Identify the blood parasite species.
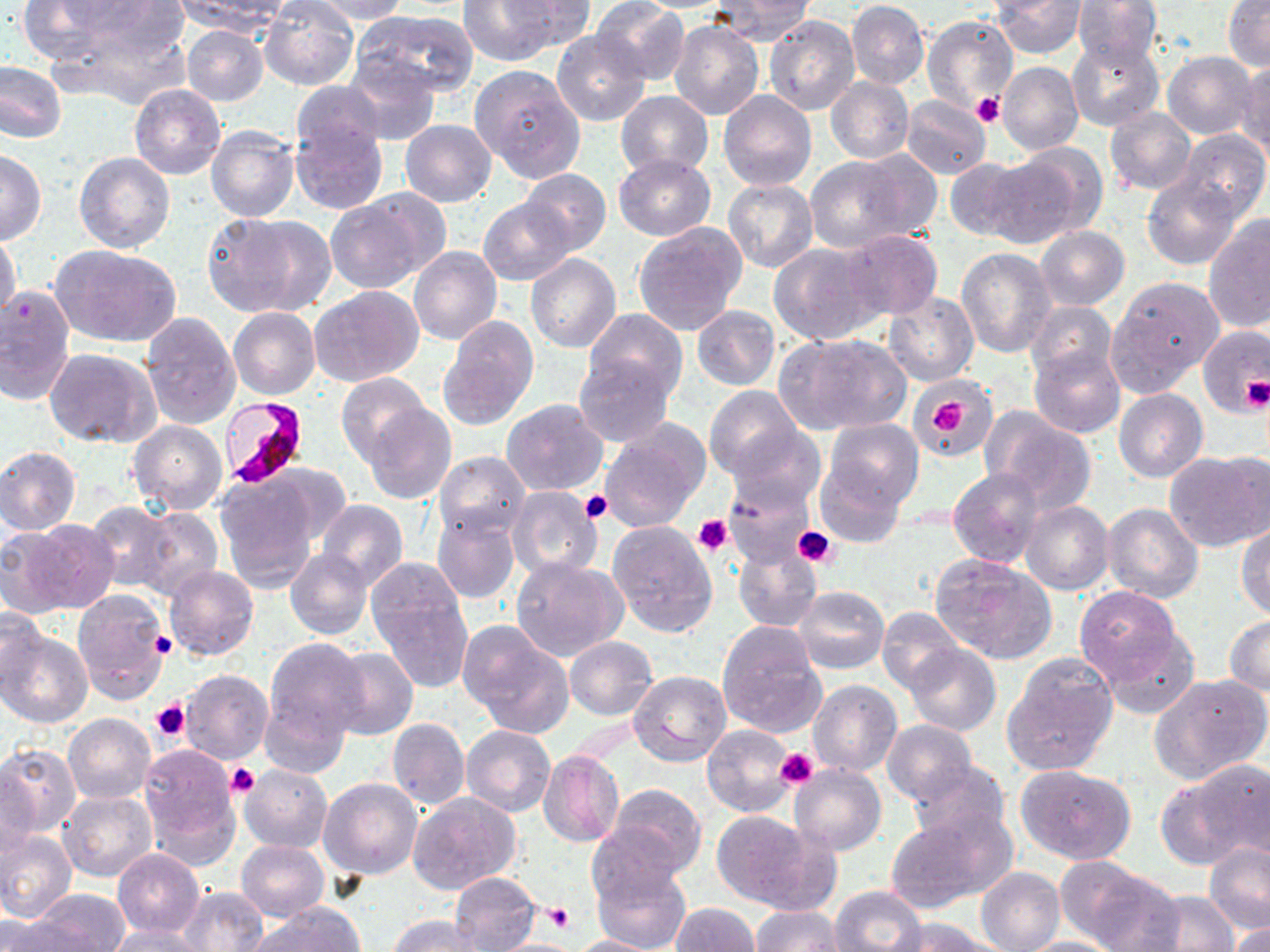
Plasmodium falciparum.

Summary:
  - Coordinate format: approximate bounding boxes as named x1/y1/x2/y2 corners in pixels
  - Uninfected red blood cell locations: (x1=16, y1=0, x2=116, y2=64), (x1=58, y1=0, x2=180, y2=53), (x1=259, y1=0, x2=359, y2=91), (x1=308, y1=0, x2=412, y2=23), (x1=456, y1=0, x2=562, y2=67), (x1=709, y1=0, x2=815, y2=45), (x1=992, y1=0, x2=1086, y2=58), (x1=1072, y1=0, x2=1162, y2=70), (x1=1223, y1=0, x2=1270, y2=70), (x1=175, y1=1, x2=292, y2=36), (x1=502, y1=1, x2=594, y2=49), (x1=592, y1=1, x2=690, y2=85), (x1=847, y1=1, x2=928, y2=89), (x1=352, y1=10, x2=478, y2=98), (x1=765, y1=15, x2=860, y2=115), (x1=922, y1=15, x2=1017, y2=113), (x1=668, y1=20, x2=765, y2=120), (x1=181, y1=25, x2=267, y2=107), (x1=551, y1=30, x2=651, y2=126), (x1=1066, y1=34, x2=1164, y2=131), (x1=1162, y1=50, x2=1259, y2=139), (x1=342, y1=56, x2=440, y2=146), (x1=0, y1=60, x2=66, y2=143), (x1=998, y1=60, x2=1084, y2=155), (x1=1236, y1=60, x2=1270, y2=154), (x1=471, y1=65, x2=585, y2=184), (x1=824, y1=77, x2=913, y2=164), (x1=289, y1=81, x2=385, y2=160), (x1=130, y1=83, x2=226, y2=179), (x1=719, y1=89, x2=816, y2=190), (x1=615, y1=91, x2=713, y2=178), (x1=902, y1=96, x2=990, y2=178), (x1=1104, y1=109, x2=1198, y2=195), (x1=400, y1=119, x2=496, y2=207), (x1=291, y1=122, x2=387, y2=215), (x1=206, y1=125, x2=299, y2=223), (x1=1178, y1=129, x2=1269, y2=220), (x1=985, y1=148, x2=1097, y2=248), (x1=0, y1=151, x2=45, y2=244), (x1=73, y1=152, x2=174, y2=254), (x1=612, y1=152, x2=716, y2=240), (x1=804, y1=156, x2=921, y2=253), (x1=944, y1=158, x2=1031, y2=242), (x1=519, y1=169, x2=610, y2=255), (x1=1142, y1=173, x2=1242, y2=269), (x1=723, y1=180, x2=819, y2=272), (x1=328, y1=192, x2=438, y2=292), (x1=478, y1=197, x2=576, y2=284), (x1=201, y1=211, x2=334, y2=319), (x1=1203, y1=218, x2=1270, y2=333), (x1=634, y1=222, x2=748, y2=335), (x1=1036, y1=225, x2=1129, y2=309), (x1=839, y1=229, x2=942, y2=321), (x1=0, y1=231, x2=20, y2=321), (x1=770, y1=241, x2=883, y2=344), (x1=52, y1=245, x2=181, y2=348), (x1=409, y1=245, x2=502, y2=344), (x1=956, y1=248, x2=1058, y2=358), (x1=525, y1=253, x2=621, y2=352), (x1=416, y1=260, x2=513, y2=410), (x1=1109, y1=277, x2=1221, y2=387), (x1=0, y1=284, x2=75, y2=405), (x1=309, y1=285, x2=423, y2=386), (x1=884, y1=291, x2=978, y2=387), (x1=1025, y1=300, x2=1118, y2=386), (x1=692, y1=306, x2=781, y2=390), (x1=228, y1=307, x2=319, y2=401), (x1=583, y1=307, x2=687, y2=402), (x1=139, y1=310, x2=241, y2=430), (x1=435, y1=315, x2=537, y2=432), (x1=1198, y1=324, x2=1270, y2=417), (x1=776, y1=333, x2=911, y2=436), (x1=1028, y1=346, x2=1124, y2=438), (x1=45, y1=348, x2=161, y2=449), (x1=572, y1=353, x2=673, y2=446), (x1=337, y1=373, x2=434, y2=468), (x1=913, y1=380, x2=999, y2=458), (x1=706, y1=386, x2=802, y2=481), (x1=1114, y1=388, x2=1208, y2=482), (x1=502, y1=398, x2=608, y2=495), (x1=361, y1=403, x2=456, y2=504), (x1=983, y1=409, x2=1096, y2=511), (x1=127, y1=419, x2=228, y2=515), (x1=822, y1=419, x2=922, y2=514), (x1=598, y1=420, x2=709, y2=531), (x1=724, y1=423, x2=826, y2=515), (x1=0, y1=446, x2=81, y2=535), (x1=1167, y1=449, x2=1269, y2=551), (x1=435, y1=451, x2=530, y2=539), (x1=816, y1=462, x2=904, y2=548), (x1=948, y1=468, x2=1045, y2=567), (x1=727, y1=472, x2=820, y2=565), (x1=213, y1=473, x2=323, y2=589), (x1=506, y1=486, x2=602, y2=582), (x1=317, y1=500, x2=407, y2=591), (x1=1020, y1=500, x2=1114, y2=595), (x1=86, y1=501, x2=180, y2=592), (x1=1101, y1=502, x2=1203, y2=602), (x1=135, y1=507, x2=222, y2=600), (x1=432, y1=511, x2=520, y2=603), (x1=22, y1=518, x2=120, y2=613), (x1=605, y1=520, x2=717, y2=638), (x1=1236, y1=523, x2=1270, y2=620), (x1=0, y1=526, x2=75, y2=619), (x1=733, y1=543, x2=822, y2=632), (x1=286, y1=547, x2=372, y2=640), (x1=930, y1=553, x2=1056, y2=664), (x1=366, y1=555, x2=471, y2=658), (x1=511, y1=557, x2=625, y2=661), (x1=164, y1=565, x2=258, y2=661), (x1=794, y1=586, x2=889, y2=674), (x1=1074, y1=586, x2=1182, y2=685), (x1=73, y1=589, x2=170, y2=705), (x1=372, y1=592, x2=473, y2=693), (x1=0, y1=606, x2=47, y2=695), (x1=877, y1=607, x2=964, y2=694), (x1=1225, y1=616, x2=1270, y2=696), (x1=716, y1=621, x2=827, y2=738), (x1=459, y1=625, x2=573, y2=735), (x1=1098, y1=628, x2=1200, y2=719), (x1=0, y1=631, x2=92, y2=727), (x1=564, y1=635, x2=657, y2=720), (x1=265, y1=636, x2=368, y2=741), (x1=905, y1=644, x2=1001, y2=736), (x1=327, y1=646, x2=418, y2=741), (x1=560, y1=646, x2=724, y2=738), (x1=1002, y1=653, x2=1118, y2=777), (x1=180, y1=670, x2=272, y2=765), (x1=629, y1=670, x2=730, y2=766), (x1=1150, y1=674, x2=1270, y2=782), (x1=807, y1=679, x2=901, y2=776), (x1=261, y1=696, x2=352, y2=779), (x1=63, y1=713, x2=156, y2=803), (x1=388, y1=717, x2=470, y2=808), (x1=881, y1=720, x2=977, y2=806), (x1=702, y1=723, x2=799, y2=817), (x1=462, y1=724, x2=554, y2=817), (x1=139, y1=743, x2=242, y2=864), (x1=0, y1=745, x2=81, y2=837), (x1=536, y1=750, x2=626, y2=848), (x1=1190, y1=759, x2=1270, y2=861), (x1=907, y1=760, x2=1012, y2=847), (x1=1015, y1=763, x2=1137, y2=864), (x1=239, y1=764, x2=332, y2=852), (x1=788, y1=764, x2=886, y2=855), (x1=1, y1=769, x2=40, y2=860), (x1=320, y1=778, x2=423, y2=881), (x1=606, y1=784, x2=706, y2=877), (x1=58, y1=791, x2=155, y2=881), (x1=407, y1=793, x2=521, y2=896), (x1=710, y1=810, x2=829, y2=912), (x1=883, y1=811, x2=1013, y2=916), (x1=585, y1=826, x2=682, y2=917), (x1=0, y1=830, x2=77, y2=923), (x1=235, y1=840, x2=328, y2=921), (x1=1204, y1=842, x2=1270, y2=935), (x1=112, y1=848, x2=205, y2=937), (x1=591, y1=859, x2=691, y2=952), (x1=1054, y1=862, x2=1173, y2=950), (x1=976, y1=867, x2=1065, y2=952), (x1=450, y1=871, x2=541, y2=950), (x1=1077, y1=874, x2=1246, y2=952), (x1=176, y1=886, x2=267, y2=951), (x1=830, y1=886, x2=926, y2=951), (x1=31, y1=890, x2=131, y2=951), (x1=1141, y1=890, x2=1239, y2=951), (x1=668, y1=903, x2=759, y2=952), (x1=751, y1=906, x2=845, y2=952), (x1=251, y1=907, x2=363, y2=952), (x1=2, y1=914, x2=70, y2=951), (x1=387, y1=915, x2=485, y2=951), (x1=887, y1=917, x2=997, y2=952), (x1=1227, y1=921, x2=1270, y2=952), (x1=103, y1=926, x2=210, y2=951), (x1=572, y1=935, x2=664, y2=952), (x1=1013, y1=937, x2=1126, y2=952), (x1=485, y1=938, x2=588, y2=952)
  - Platelet locations: (x1=971, y1=91, x2=1003, y2=129), (x1=1242, y1=377, x2=1269, y2=411), (x1=930, y1=397, x2=967, y2=436), (x1=579, y1=488, x2=612, y2=524), (x1=692, y1=515, x2=732, y2=555), (x1=794, y1=524, x2=837, y2=568), (x1=152, y1=633, x2=178, y2=659), (x1=151, y1=698, x2=191, y2=742), (x1=776, y1=747, x2=820, y2=789), (x1=226, y1=762, x2=259, y2=799), (x1=545, y1=901, x2=571, y2=931)
  - Plasmodium falciparum-infected red blood cell locations: (x1=221, y1=397, x2=309, y2=488)
  - Modality: optical microscopy
  - Stain: May-Grünwald-Giemsa
  - Field of view: one of a larger specimen
  - Preparation: thin blood film
  - Magnification: 1000x
  - Image size: 1270×952 pixels